Locate and identify every blood parasite.
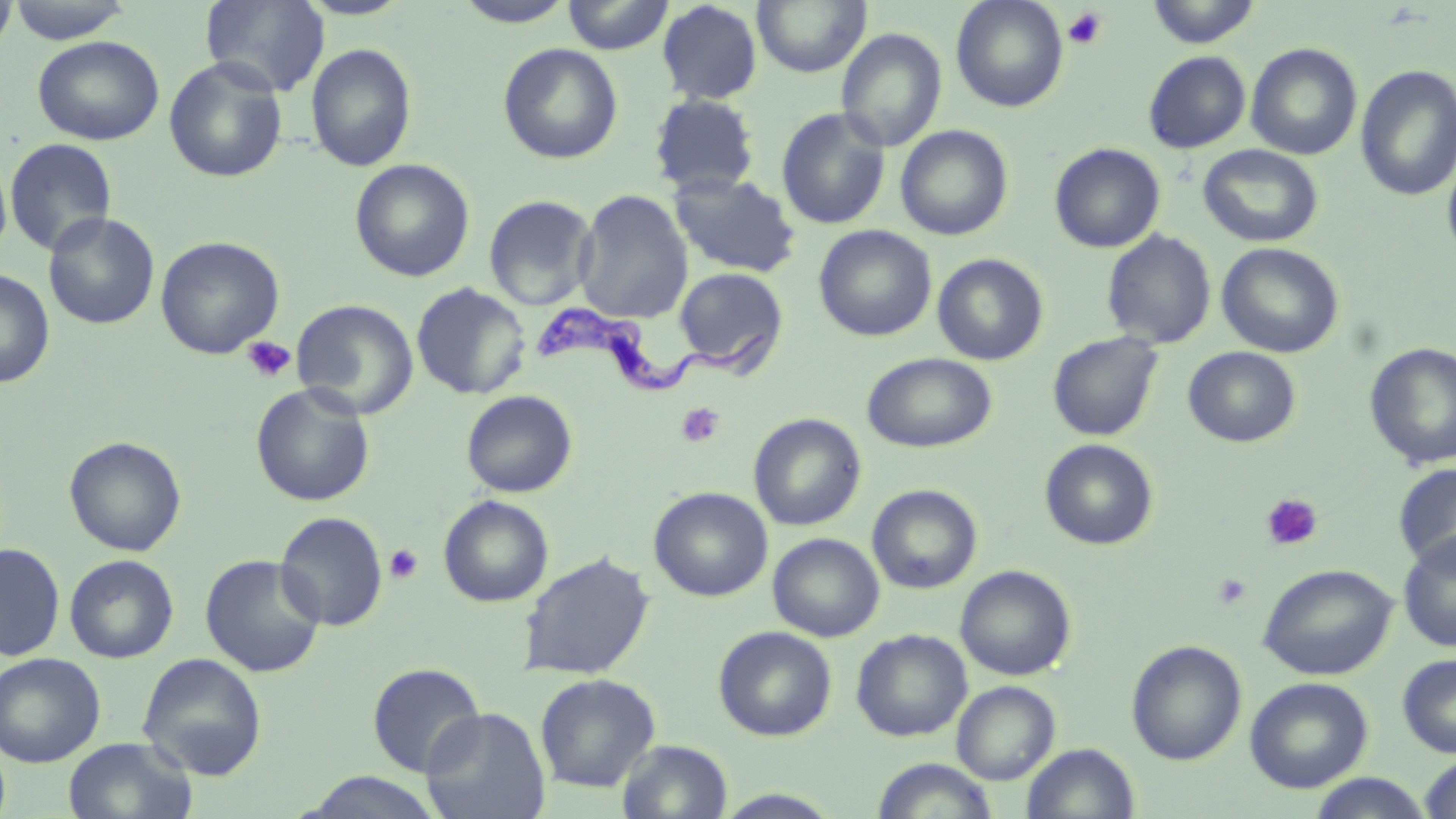

Approximate bounding boxes as named x1/y1/x2/y2 corners in pixels.
Trypanosoma brucei: (x1=533, y1=293, x2=775, y2=396).
No Plasmodium falciparum, Plasmodium ovale, Plasmodium malariae, Plasmodium vivax, or Babesia divergens observed.

{
  "slide_level_diagnosis": "Trypanosoma brucei",
  "modality": "light microscopy",
  "magnification": "1000x",
  "field_of_view": "single",
  "preparation": "thin blood film",
  "image_size": "1456×819 pixels",
  "platelet_locations": "approximate bounding boxes as named x1/y1/x2/y2 corners in pixels: (x1=1062, y1=7, x2=1108, y2=50), (x1=241, y1=334, x2=296, y2=383), (x1=676, y1=402, x2=724, y2=448), (x1=1260, y1=493, x2=1324, y2=552), (x1=384, y1=544, x2=423, y2=585), (x1=1212, y1=572, x2=1253, y2=610)",
  "stain": "May-Grünwald-Giemsa",
  "uninfected_red_blood_cell_locations": "approximate bounding boxes as named x1/y1/x2/y2 corners in pixels: (x1=6, y1=0, x2=135, y2=43), (x1=200, y1=0, x2=329, y2=96), (x1=296, y1=0, x2=414, y2=20), (x1=562, y1=0, x2=674, y2=54), (x1=752, y1=0, x2=871, y2=76), (x1=950, y1=0, x2=1069, y2=112), (x1=1145, y1=0, x2=1262, y2=48), (x1=0, y1=1, x2=18, y2=56), (x1=451, y1=1, x2=577, y2=27), (x1=656, y1=1, x2=763, y2=104), (x1=836, y1=28, x2=947, y2=152), (x1=32, y1=35, x2=165, y2=145), (x1=305, y1=43, x2=416, y2=172), (x1=498, y1=43, x2=623, y2=164), (x1=1246, y1=43, x2=1363, y2=160), (x1=1143, y1=51, x2=1251, y2=153), (x1=163, y1=57, x2=288, y2=183), (x1=1355, y1=64, x2=1456, y2=202), (x1=649, y1=93, x2=761, y2=196), (x1=776, y1=107, x2=891, y2=230), (x1=895, y1=124, x2=1013, y2=241), (x1=4, y1=138, x2=118, y2=256), (x1=1049, y1=143, x2=1165, y2=253), (x1=1198, y1=144, x2=1324, y2=248), (x1=1442, y1=146, x2=1456, y2=267), (x1=0, y1=158, x2=12, y2=263), (x1=350, y1=158, x2=475, y2=282), (x1=669, y1=172, x2=802, y2=278), (x1=573, y1=189, x2=693, y2=324), (x1=483, y1=194, x2=598, y2=310), (x1=43, y1=212, x2=161, y2=330), (x1=814, y1=225, x2=937, y2=341), (x1=1101, y1=230, x2=1217, y2=349), (x1=154, y1=235, x2=285, y2=359), (x1=1216, y1=242, x2=1344, y2=358), (x1=932, y1=253, x2=1049, y2=365), (x1=672, y1=267, x2=790, y2=375), (x1=0, y1=268, x2=55, y2=389), (x1=411, y1=282, x2=530, y2=400), (x1=291, y1=299, x2=419, y2=420), (x1=1046, y1=331, x2=1164, y2=442), (x1=1364, y1=342, x2=1456, y2=469), (x1=1183, y1=346, x2=1301, y2=448), (x1=861, y1=352, x2=997, y2=453), (x1=250, y1=383, x2=375, y2=506), (x1=461, y1=390, x2=577, y2=497), (x1=748, y1=412, x2=867, y2=531), (x1=64, y1=435, x2=187, y2=556), (x1=1039, y1=438, x2=1159, y2=550), (x1=1393, y1=463, x2=1456, y2=570), (x1=867, y1=484, x2=982, y2=594), (x1=648, y1=486, x2=773, y2=602), (x1=438, y1=494, x2=554, y2=607), (x1=275, y1=511, x2=388, y2=631), (x1=1398, y1=531, x2=1456, y2=652), (x1=768, y1=533, x2=884, y2=641), (x1=0, y1=543, x2=65, y2=661), (x1=517, y1=552, x2=654, y2=680), (x1=65, y1=554, x2=179, y2=663), (x1=200, y1=554, x2=326, y2=677), (x1=1258, y1=563, x2=1397, y2=680), (x1=955, y1=565, x2=1076, y2=681), (x1=713, y1=626, x2=837, y2=741), (x1=851, y1=629, x2=973, y2=742), (x1=1126, y1=640, x2=1247, y2=765), (x1=0, y1=652, x2=106, y2=768), (x1=137, y1=652, x2=267, y2=780), (x1=1397, y1=653, x2=1456, y2=758), (x1=367, y1=662, x2=486, y2=777), (x1=535, y1=673, x2=660, y2=793), (x1=1245, y1=676, x2=1373, y2=793), (x1=951, y1=680, x2=1060, y2=784), (x1=420, y1=706, x2=551, y2=819), (x1=63, y1=737, x2=197, y2=819), (x1=617, y1=739, x2=733, y2=819), (x1=1022, y1=743, x2=1140, y2=819), (x1=1419, y1=754, x2=1456, y2=819), (x1=872, y1=758, x2=999, y2=819), (x1=296, y1=771, x2=446, y2=818), (x1=1306, y1=773, x2=1435, y2=818), (x1=713, y1=788, x2=844, y2=818)"
}